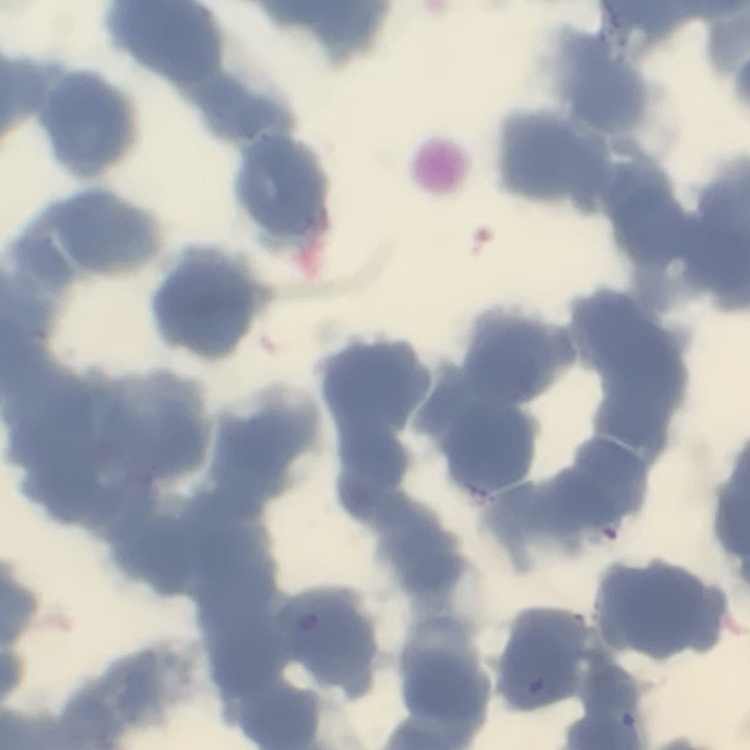

The erythrocytes show rouleaux formation. Thin blood film. One tile cut from a larger photomicrograph. Stained with either Field's or Giemsa.